Comment on the morphology of the red blood cells.
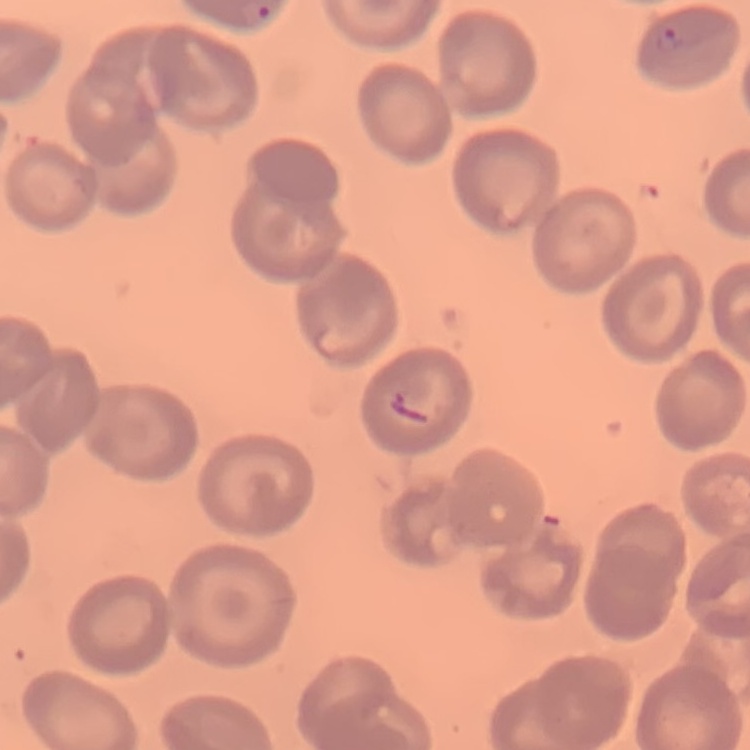

They show no rouleaux formation.

Thin peripheral smear. One tile cut from a larger photomicrograph. Field's or Giemsa stain.